Report the malaria status of this cell.
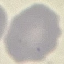

It is uninfected.

capture = smartphone through the microscope eyepiece
preparation = thin blood smear
stain = Giemsa
image type = automatically extracted cell patch, resized to 64 × 64 pixels